State which parasite is depicted.
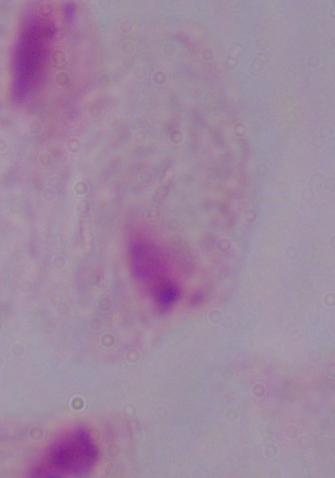

This is a trichomonad.

Captured at 1000x magnification. Photomicrograph.